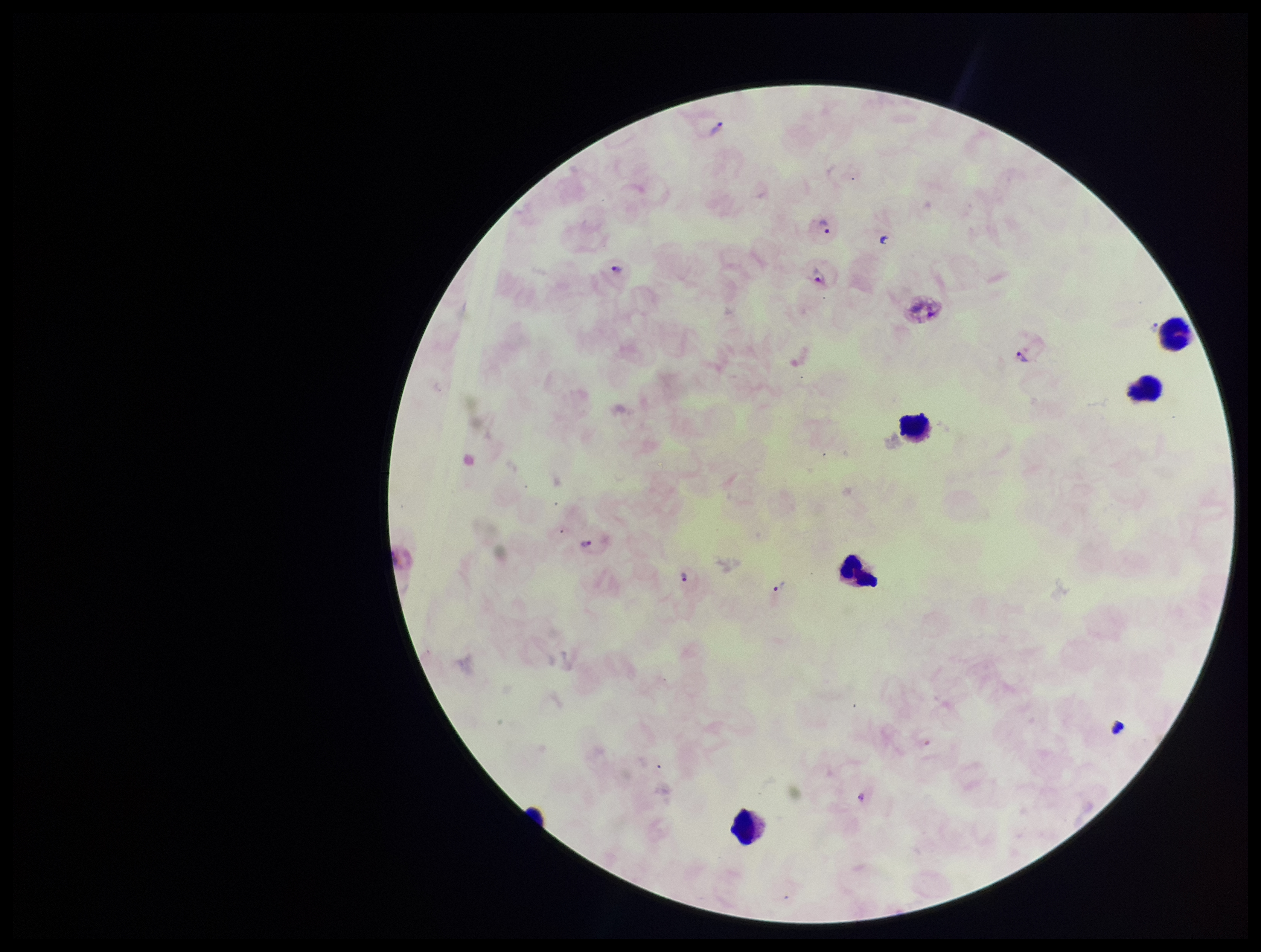

{
  "plasmodium_parasites": "detected",
  "preparation": "thick smear",
  "species_reported_for_this_patient": "Plasmodium vivax",
  "patient_malaria_status": "infected",
  "image_size": "1261×952 pixels",
  "field_of_view": "one from this slide",
  "stain": "Giemsa",
  "capture": "smartphone photograph through the microscope eyepiece",
  "parasite_count": 7,
  "leukocyte_count": 5
}